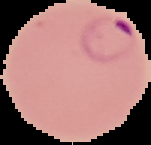

malaria_status: parasitized
image_size: 151×145 pixels
image_type: segmented cell region with the area outside set to black
preparation: thin blood film